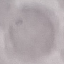
Summary:
  - Malaria status: uninfected
  - Image type: cell patch, automatically extracted from a larger field of view and resized to 64 × 64 pixels
  - Capture: smartphone camera at the microscope eyepiece
  - Stain: Giemsa
  - Preparation: thin blood smear